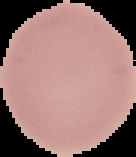
Summary:
  - Image size: 136×157 pixels
  - Preparation: thin blood film
  - Image type: segmented cell region on a black background
  - Result: negative for malaria parasites